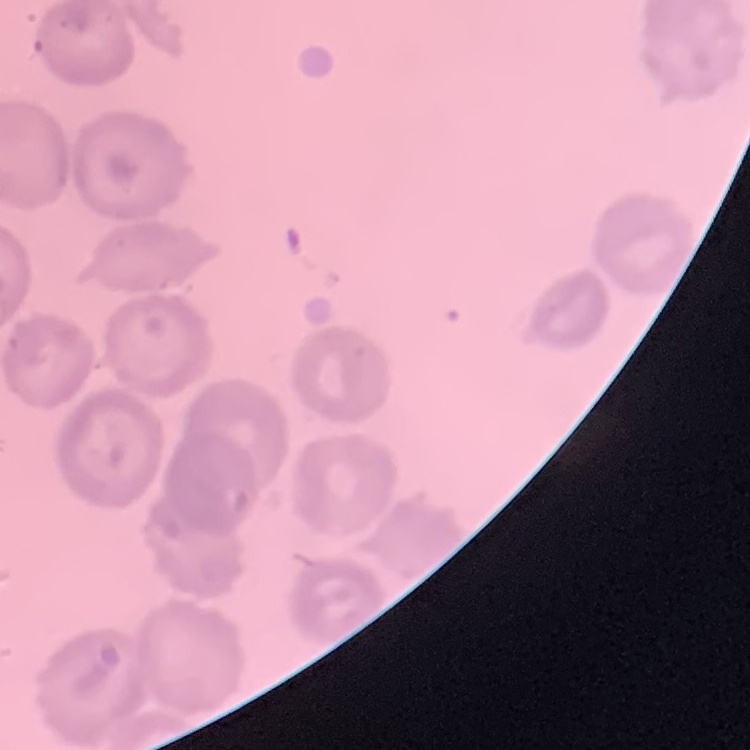

The red blood cells show no rouleaux formation. One tile cut from a larger photomicrograph. Thin peripheral smear. Field's or Giemsa stain.